Classify this cell by malaria status.
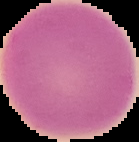
Uninfected.

Image is 139×142 pixels. From a thin blood film. Cell region segmented out of the field of view; the surrounding area is masked to black.